Describe the morphology of the erythrocytes.
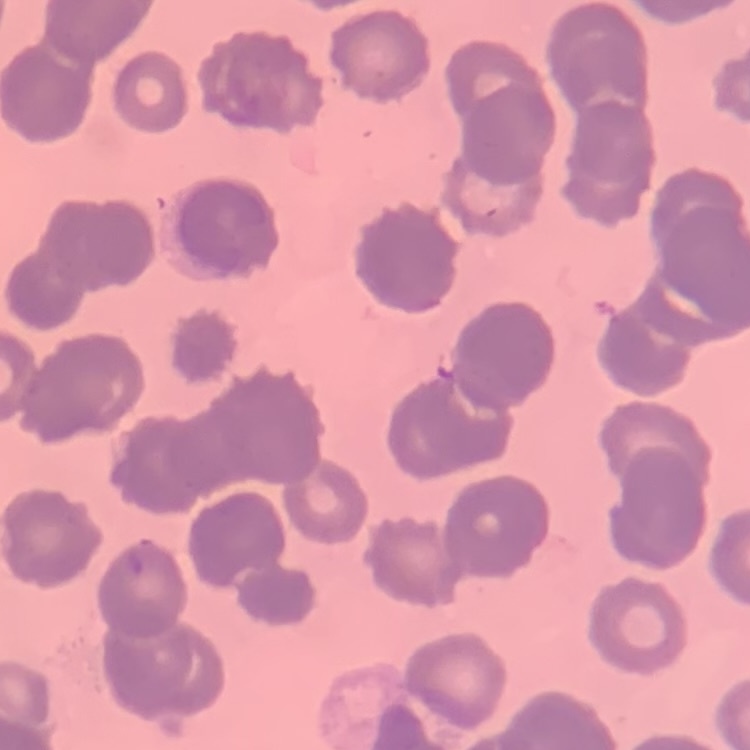
They show rouleaux formation.

image type = one tile cut from a larger photomicrograph
preparation = thin peripheral smear
stain = Field's or Giemsa